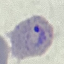
Summary:
  - Result: malaria parasites detected
  - Image type: cell patch, automatically extracted from a larger field of view and resized to 64 × 64 pixels
  - Capture: smartphone through the microscope eyepiece
  - Stain: Giemsa
  - Preparation: thin blood film